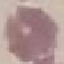

Summary:
  - Result: no malaria parasites detected
  - Capture: smartphone camera at the microscope eyepiece
  - Image type: automatically extracted cell patch, resized to 64 × 64 pixels
  - Preparation: thin smear
  - Stain: Giemsa